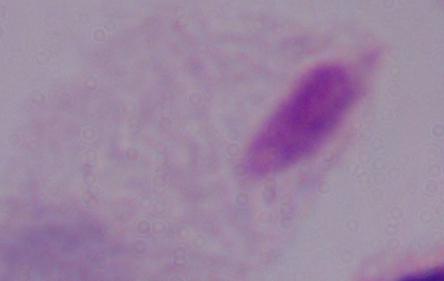
{
  "magnification": "1000x",
  "modality": "photomicrograph",
  "identification": "trichomonad"
}